Identify the parasite.
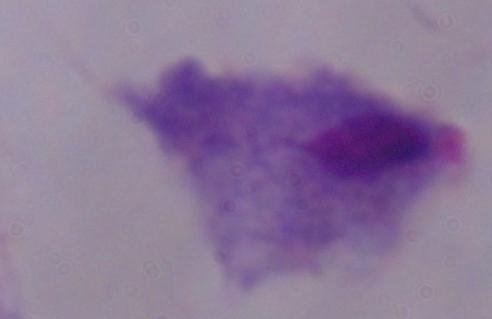
This is a trichomonad.

Summary:
  - Magnification: 1000x
  - Modality: photomicrograph